Report the malaria status of this cell.
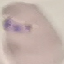
It is parasitized.

Summary:
  - Preparation: thin blood film
  - Capture: smartphone through the microscope eyepiece
  - Stain: Giemsa
  - Image type: automatically extracted cell patch, resized to 64 × 64 pixels